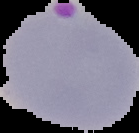

preparation = thin blood smear
image size = 139×133 pixels
malaria status = parasitized
image type = segmented cell region with the area outside set to black